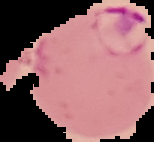
Summary:
  - Preparation: thin blood smear
  - Image size: 154×142 pixels
  - Image type: cell region segmented out of the field of view; surrounding area masked to black
  - Malaria status: parasitized